State which parasite is depicted.
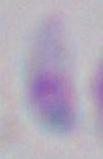

This is Toxoplasma gondii.

Micrograph. Captured at 1000x magnification.